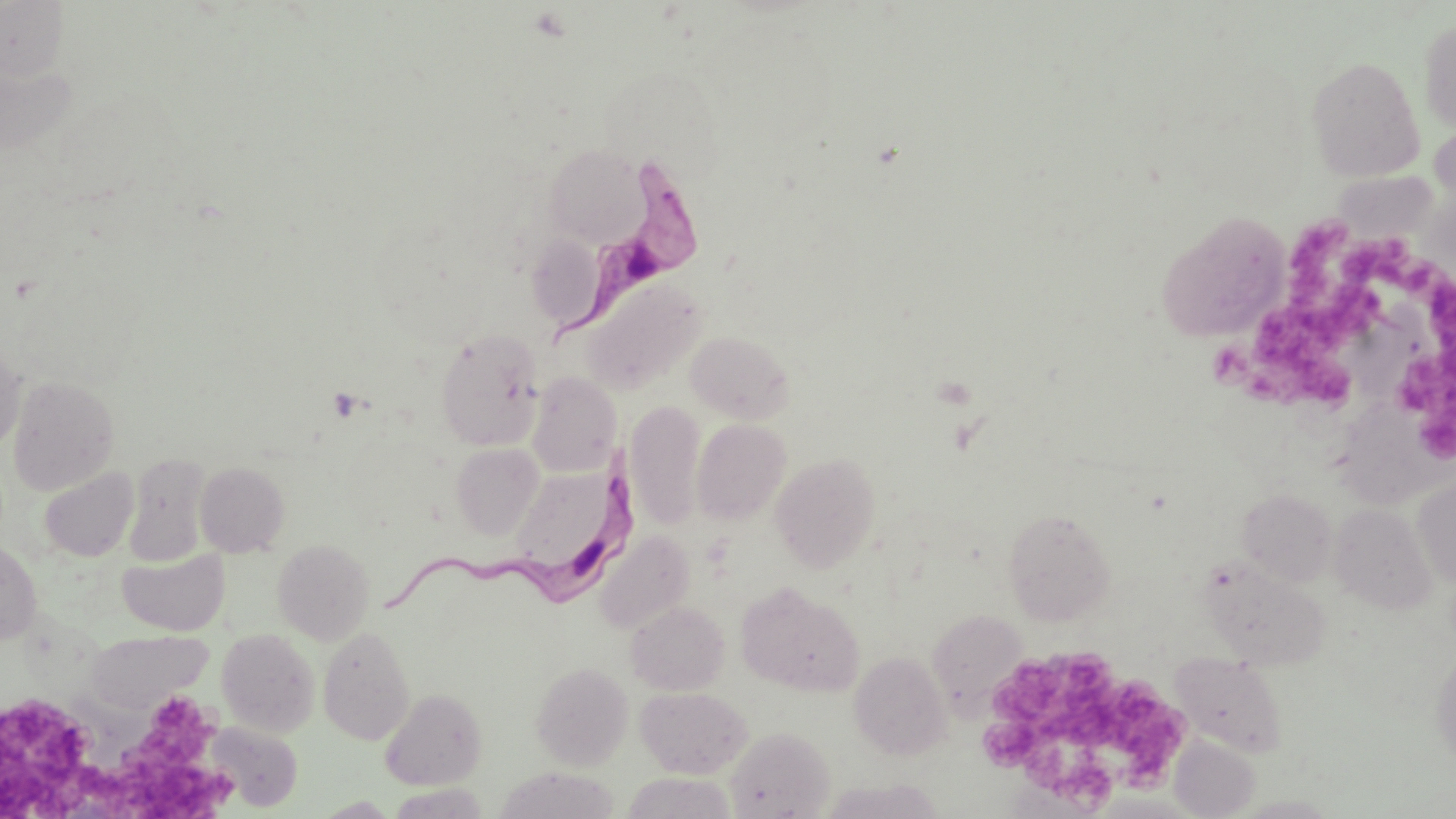
Summary:
  - Coordinate format: approximate bounding boxes as [x1, y1, x2, y2] in pixels
  - Platelet locations: [1283, 218, 1354, 318], [1347, 236, 1444, 300], [1418, 277, 1456, 349], [1321, 278, 1397, 338], [1208, 313, 1362, 411], [1393, 346, 1456, 460], [987, 648, 1130, 747], [1093, 676, 1188, 778], [0, 690, 113, 815], [107, 690, 233, 819], [976, 714, 1042, 759], [1058, 751, 1121, 813]
  - Uninfected red blood cell locations: [0, 0, 70, 82], [1418, 17, 1456, 133], [1306, 55, 1425, 181], [0, 60, 80, 157], [543, 144, 646, 247], [1160, 214, 1291, 342], [526, 234, 609, 332], [580, 277, 706, 395], [436, 329, 545, 451], [685, 330, 794, 423], [0, 343, 25, 451], [527, 372, 621, 476], [8, 375, 120, 496], [1341, 395, 1434, 507], [626, 400, 705, 529], [692, 419, 791, 525], [451, 443, 545, 540], [771, 453, 881, 573], [123, 454, 212, 566], [196, 461, 290, 557], [506, 462, 633, 588], [39, 467, 139, 561], [1412, 476, 1456, 588], [1238, 488, 1337, 586], [1330, 503, 1437, 613], [1003, 507, 1117, 625], [595, 531, 694, 633], [273, 539, 374, 644], [0, 541, 42, 645], [117, 549, 229, 635], [1199, 556, 1335, 674], [737, 583, 864, 696], [627, 601, 730, 695], [927, 609, 1027, 708], [318, 626, 415, 744], [216, 628, 320, 737], [86, 629, 212, 714], [1430, 648, 1456, 769], [849, 651, 951, 760], [1169, 651, 1288, 757], [531, 661, 633, 769], [636, 686, 752, 777], [380, 688, 487, 789], [206, 722, 302, 811], [725, 727, 835, 818], [1169, 735, 1260, 818], [495, 767, 620, 819], [822, 779, 944, 819], [314, 796, 400, 818], [1235, 796, 1343, 818]
  - Trypanosoma brucei locations: [555, 151, 706, 356], [381, 447, 643, 627]
  - Slide-level diagnosis: Trypanosoma brucei
  - Image size: 1456×819 pixels
  - Preparation: thin blood film
  - Field of view: one of a larger specimen
  - Modality: light microscopy
  - Magnification: 1000x
  - Stain: May-Grünwald-Giemsa